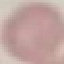
Summary:
  - Malaria status: uninfected
  - Capture: smartphone camera at the microscope eyepiece
  - Stain: Giemsa
  - Preparation: thin blood film
  - Image type: automatically extracted cell patch, resized to 64 × 64 pixels